Report the malaria status of this cell.
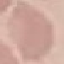
It is uninfected.

{
  "preparation": "thin blood film",
  "stain": "Giemsa",
  "capture": "smartphone through the microscope eyepiece",
  "image_type": "cell patch, automatically extracted from a larger field of view and resized to 64 × 64 pixels"
}